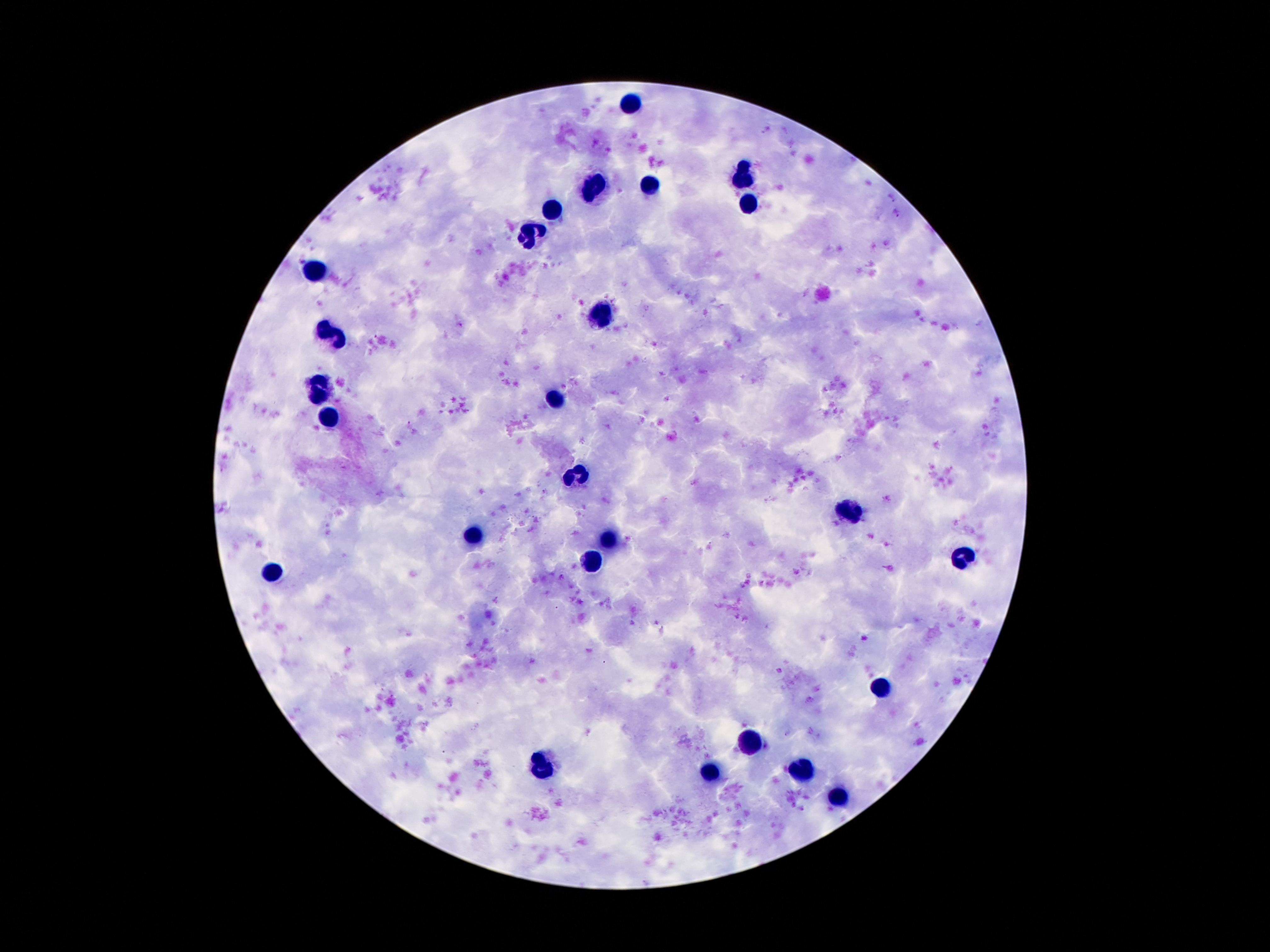

Approximate centers as [x, y] in pixels.
Summary:
  - Leukocyte locations: [628, 104], [744, 180], [650, 186], [597, 189], [552, 209], [748, 212], [529, 238], [314, 268], [599, 314], [333, 333], [320, 389], [558, 400], [328, 417], [576, 475], [851, 512], [470, 536], [609, 544], [964, 559], [589, 564], [269, 571], [882, 686], [750, 743], [541, 769], [800, 772], [712, 773], [839, 797]
  - Field of view: single
  - Image size: 1270×952 pixels
  - Magnification: 100x
  - Capture: smartphone camera through the microscope eyepiece
  - Stain: Giemsa
  - Preparation: thick blood film
  - Patient malaria status: negative